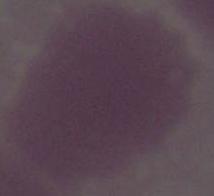
Summary:
  - Identification: red blood cell
  - Modality: photomicrograph
  - Magnification: 1000x